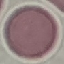
Summary:
  - Malaria status: uninfected
  - Stain: Giemsa
  - Capture: smartphone camera at the microscope eyepiece
  - Preparation: thin blood film
  - Image type: cell patch, automatically extracted from a larger field of view and resized to 64 × 64 pixels